Outline each Plasmodium falciparum-infected red blood cell.
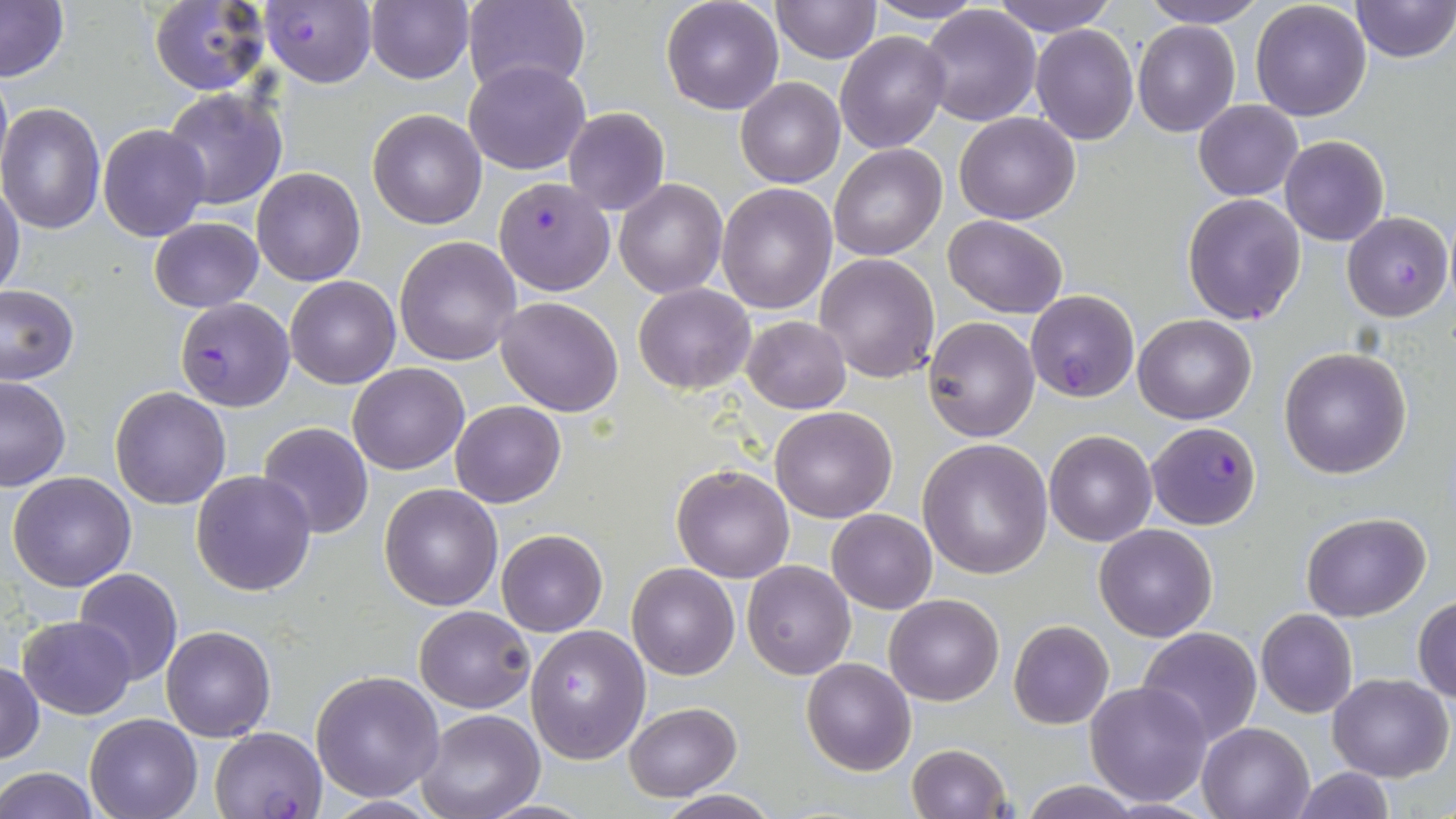

Approximate bounding boxes as (x1,y1)-(x2,y2) corner pairs in pixels.
Plasmodium falciparum-infected red blood cells: (260,0)-(376,87), (492,177)-(615,296), (1342,210)-(1453,321), (1025,289)-(1139,402), (175,297)-(295,411), (1148,421)-(1259,530), (210,726)-(327,818).

Uninfected red blood cell locations: (365,0)-(473,84), (463,0)-(589,96), (660,0)-(785,116), (863,0)-(986,26), (992,0)-(1118,35), (1142,0)-(1267,27), (1250,0)-(1371,121), (1352,0)-(1454,63), (1,1)-(68,83), (148,1)-(269,96), (770,1)-(881,64), (919,5)-(1042,127), (1132,20)-(1241,137), (1031,25)-(1140,147), (835,30)-(951,153), (465,60)-(589,174), (0,67)-(12,184), (735,77)-(846,188), (161,86)-(288,212), (1193,100)-(1302,200), (0,101)-(106,233), (563,107)-(669,216), (368,109)-(488,229), (954,112)-(1080,225), (98,124)-(210,240), (1280,135)-(1388,247), (829,143)-(946,260), (251,168)-(364,285), (614,177)-(727,298), (0,181)-(25,303), (716,183)-(838,315), (1182,193)-(1307,324), (943,215)-(1066,318), (149,218)-(262,312), (394,236)-(521,365), (815,253)-(941,382), (284,276)-(399,388), (634,284)-(754,394), (0,286)-(78,383), (495,296)-(625,417), (1133,314)-(1255,423), (742,315)-(851,414), (922,316)-(1039,442), (1279,346)-(1412,479), (348,362)-(469,475), (0,374)-(70,491), (110,387)-(231,511), (450,400)-(566,508), (769,405)-(897,522), (259,421)-(373,538), (1043,429)-(1157,546), (918,438)-(1053,580), (672,463)-(796,583), (190,470)-(316,596), (7,473)-(136,591), (379,483)-(503,610), (826,507)-(938,613), (1301,512)-(1431,621), (1094,523)-(1218,641), (496,529)-(607,637), (742,560)-(856,680), (627,563)-(739,680), (74,569)-(183,685), (884,593)-(1004,705), (1412,596)-(1456,703), (414,605)-(536,712), (1256,609)-(1358,717), (18,614)-(137,719), (1008,620)-(1113,730), (525,623)-(651,764), (161,625)-(276,741), (1136,626)-(1264,748), (801,657)-(917,775), (0,664)-(44,762), (311,670)-(445,800), (1328,673)-(1453,781), (1083,680)-(1213,806), (623,702)-(741,799), (417,710)-(546,819), (84,714)-(201,819), (1196,721)-(1313,819), (905,744)-(1011,819), (1291,766)-(1397,819), (1,767)-(100,819), (1017,780)-(1144,819), (655,791)-(781,818), (320,796)-(446,817). Slide-level diagnosis: Plasmodium falciparum. Image is 1456×819 pixels. Captured at 1000x magnification. May-Grünwald-Giemsa stain. Light microscopy. One field of a larger specimen. Thin blood film.